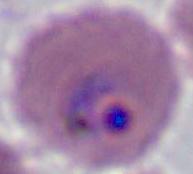
magnification = 400x or 1000x
modality = photomicrograph
identification = Plasmodium